Identify the cell.
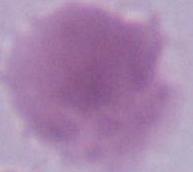
An erythrocyte.

Summary:
  - Modality: micrograph
  - Magnification: 1000x